Locate and identify every blood parasite.
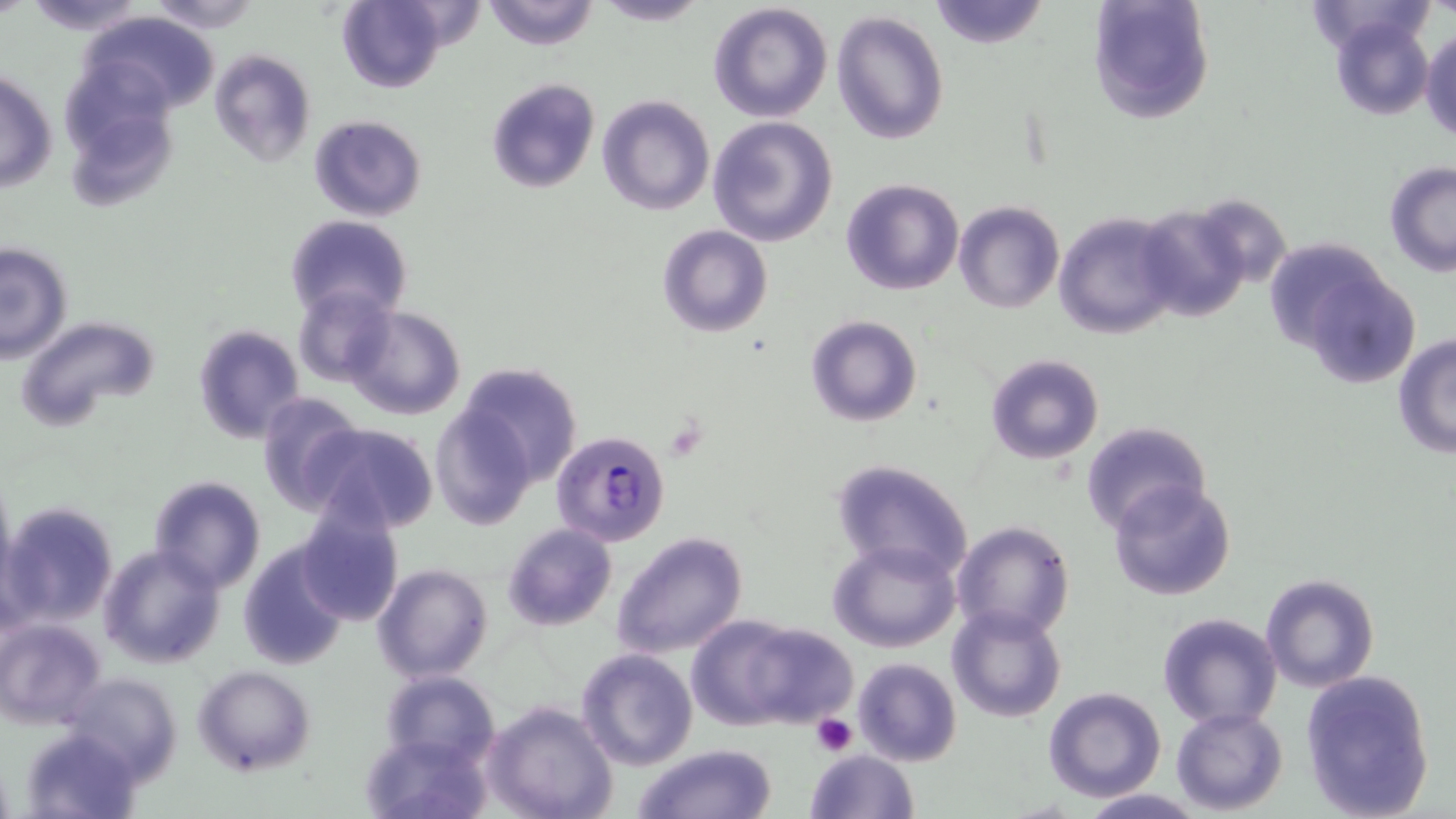
Approximate bounding boxes as (x1, y1, x2, y2) in pixels.
Plasmodium falciparum-infected red blood cells: (551, 431, 670, 546).
No Plasmodium ovale, Plasmodium malariae, Plasmodium vivax, Babesia divergens, or Trypanosoma brucei observed.

slide-level diagnosis = Plasmodium falciparum
platelet locations = approximate bounding boxes as (x1, y1, x2, y2) in pixels: (811, 713, 857, 757)
uninfected red blood cell locations = approximate bounding boxes as (x1, y1, x2, y2) in pixels: (21, 0, 153, 37), (482, 0, 600, 51), (587, 0, 712, 26), (926, 0, 1051, 52), (1088, 0, 1214, 124), (144, 1, 261, 32), (708, 1, 834, 121), (339, 2, 449, 93), (832, 10, 951, 145), (84, 11, 220, 116), (1330, 12, 1435, 121), (1421, 28, 1455, 144), (52, 47, 176, 173), (208, 48, 317, 166), (1, 68, 56, 194), (485, 77, 599, 195), (597, 93, 716, 217), (308, 114, 427, 222), (707, 115, 838, 247), (76, 131, 184, 212), (1383, 162, 1456, 276), (840, 178, 963, 294), (953, 202, 1063, 314), (1131, 202, 1254, 324), (1055, 211, 1182, 340), (287, 215, 413, 323), (657, 225, 773, 338), (0, 242, 72, 364), (1283, 246, 1424, 385), (294, 287, 397, 386), (344, 306, 466, 421), (807, 315, 922, 426), (14, 316, 159, 434), (192, 324, 304, 443), (1392, 335, 1456, 459), (985, 354, 1104, 465), (455, 360, 584, 488), (254, 393, 363, 514), (430, 404, 536, 530), (1080, 420, 1212, 535), (304, 421, 440, 535), (830, 458, 975, 582), (148, 475, 266, 594), (1108, 478, 1237, 602), (2, 501, 119, 627), (297, 508, 404, 626), (951, 520, 1076, 640), (502, 523, 617, 632), (613, 531, 749, 659), (238, 538, 353, 671), (828, 538, 961, 653), (98, 543, 224, 668), (371, 563, 492, 684), (1260, 573, 1381, 693), (947, 605, 1067, 723), (1157, 611, 1284, 731), (1, 616, 107, 729), (686, 616, 804, 731), (741, 621, 857, 726), (576, 648, 697, 771), (852, 658, 961, 767), (192, 665, 316, 777), (1300, 669, 1436, 819), (378, 670, 500, 767), (61, 672, 181, 781), (1042, 686, 1166, 802), (483, 700, 618, 819), (1173, 707, 1288, 815), (23, 728, 145, 819), (361, 730, 494, 819), (635, 744, 778, 819), (804, 747, 917, 819), (1076, 789, 1204, 819)
image size = 1456×819 pixels
stain = May-Grünwald-Giemsa
magnification = 1000x
modality = optical microscopy
preparation = thin blood film
field of view = one of a larger specimen